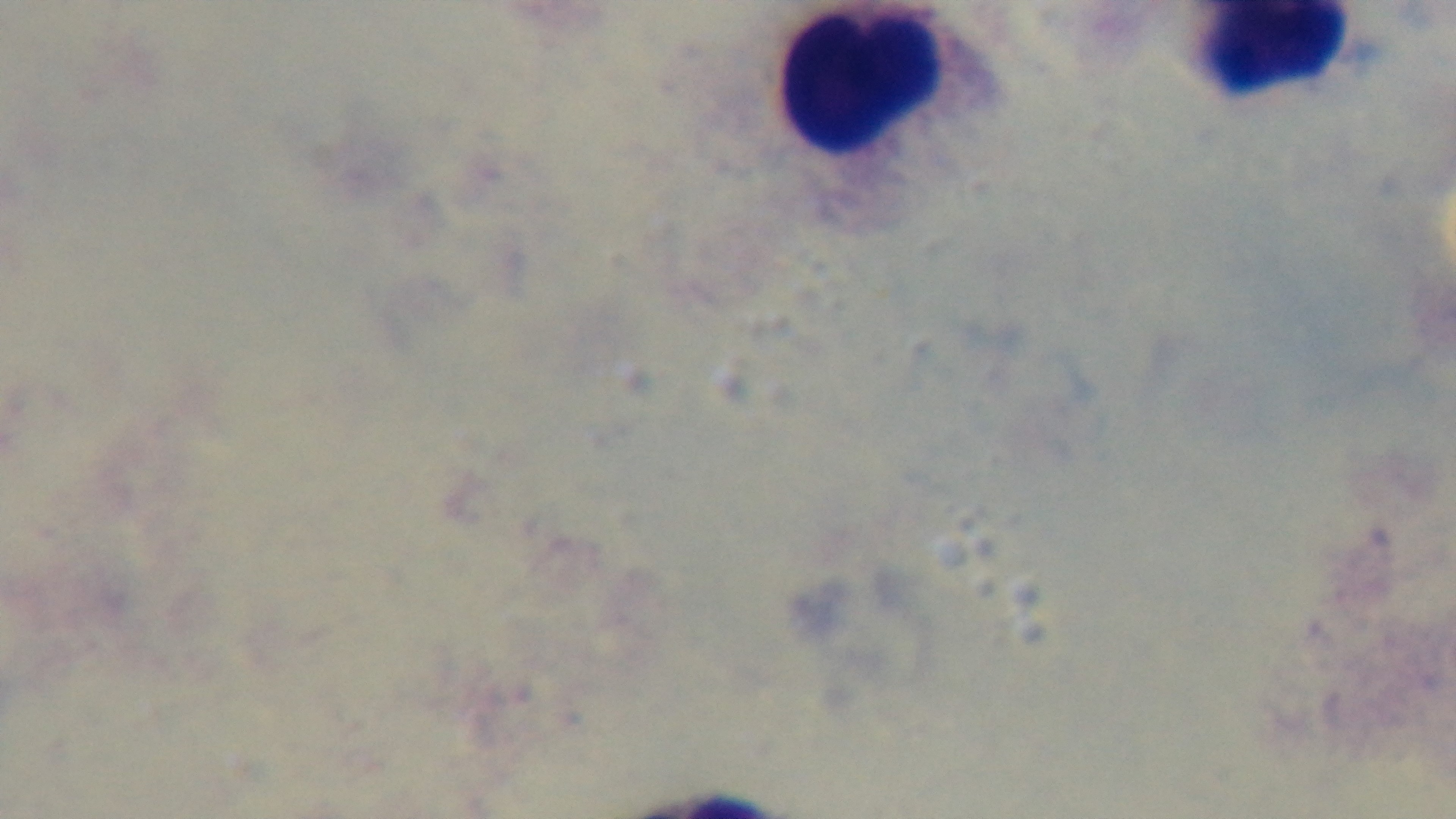

Malaria status: uninfected. Giemsa stain. Captured with a mounted 4K digital camera. Photomicrograph. Preparation: thick blood film. One field from the slide. Oil-immersion objective, 100x.